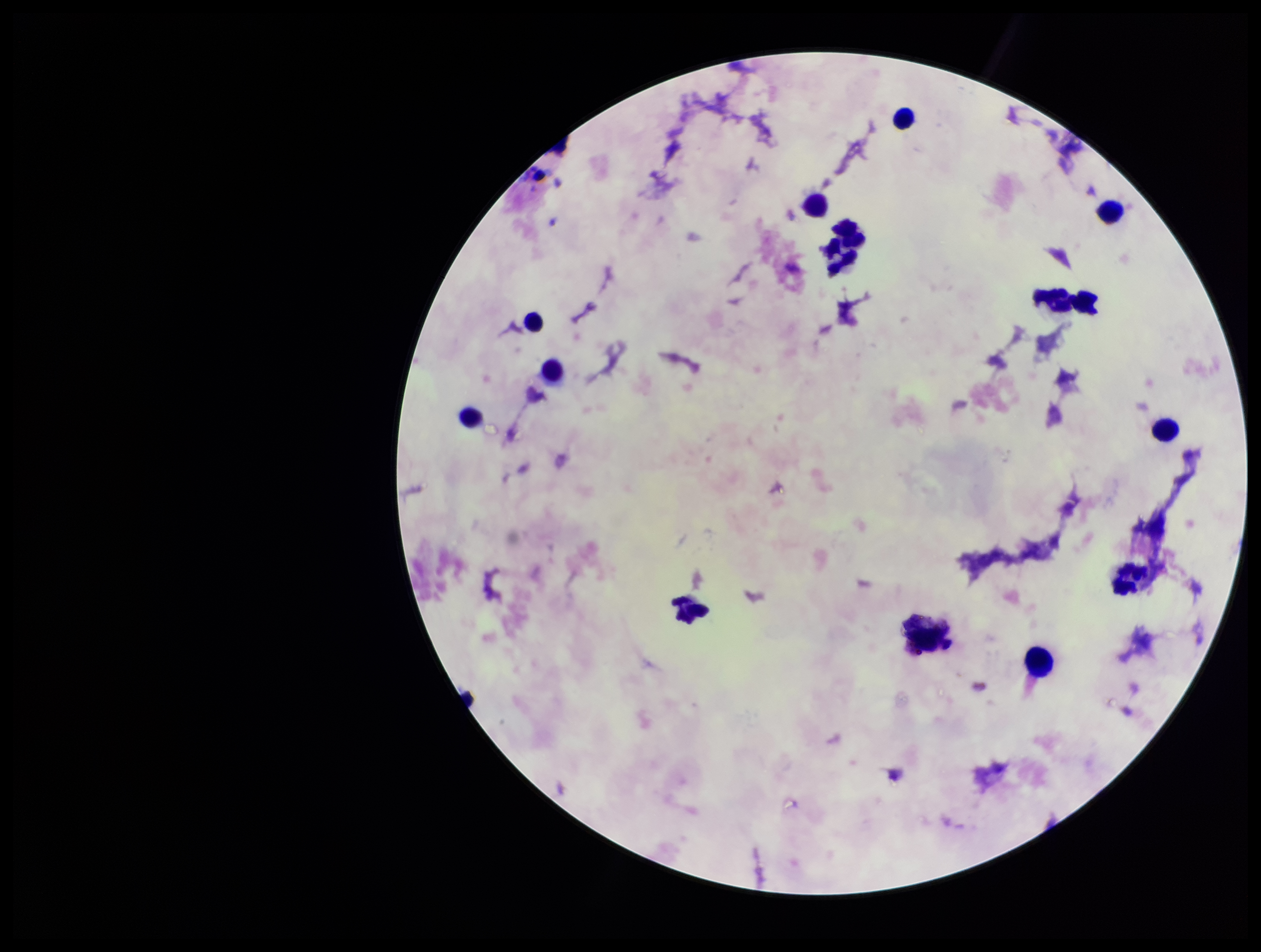
Summary:
  - Image size: 1261×952 pixels
  - Plasmodium parasites: none detected
  - Capture: smartphone photograph through the microscope eyepiece
  - Preparation: thick
  - Field of view: single
  - Stain: Giemsa
  - Parasite count: 0
  - Leukocyte count: 13
  - Patient malaria status: negative